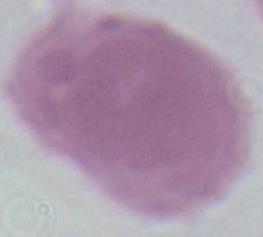 Photomicrograph. An erythrocyte is shown. Captured at 1000x magnification.